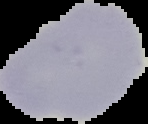
Summary:
  - Image size: 148×124 pixels
  - Result: no Plasmodium parasites detected
  - Image type: segmented cell region on a black background
  - Preparation: thin blood film